Identify the cell.
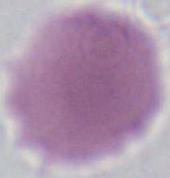
An erythrocyte.

modality: micrograph
magnification: 1000x